Assess this cell for malaria.
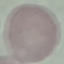
It is uninfected.

Summary:
  - Stain: Giemsa
  - Preparation: thin blood smear
  - Image type: cell patch, automatically extracted from a larger field of view and resized to 64 × 64 pixels
  - Capture: smartphone through the microscope eyepiece